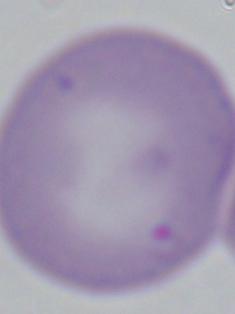 A Babesia parasite is seen. Micrograph. Captured at 1000x magnification.